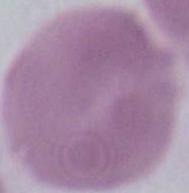

{
  "modality": "micrograph",
  "identification": "red blood cell",
  "magnification": "1000x"
}